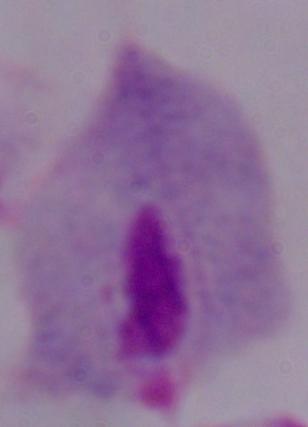

Captured at 1000x magnification. A trichomonad is seen. Micrograph.